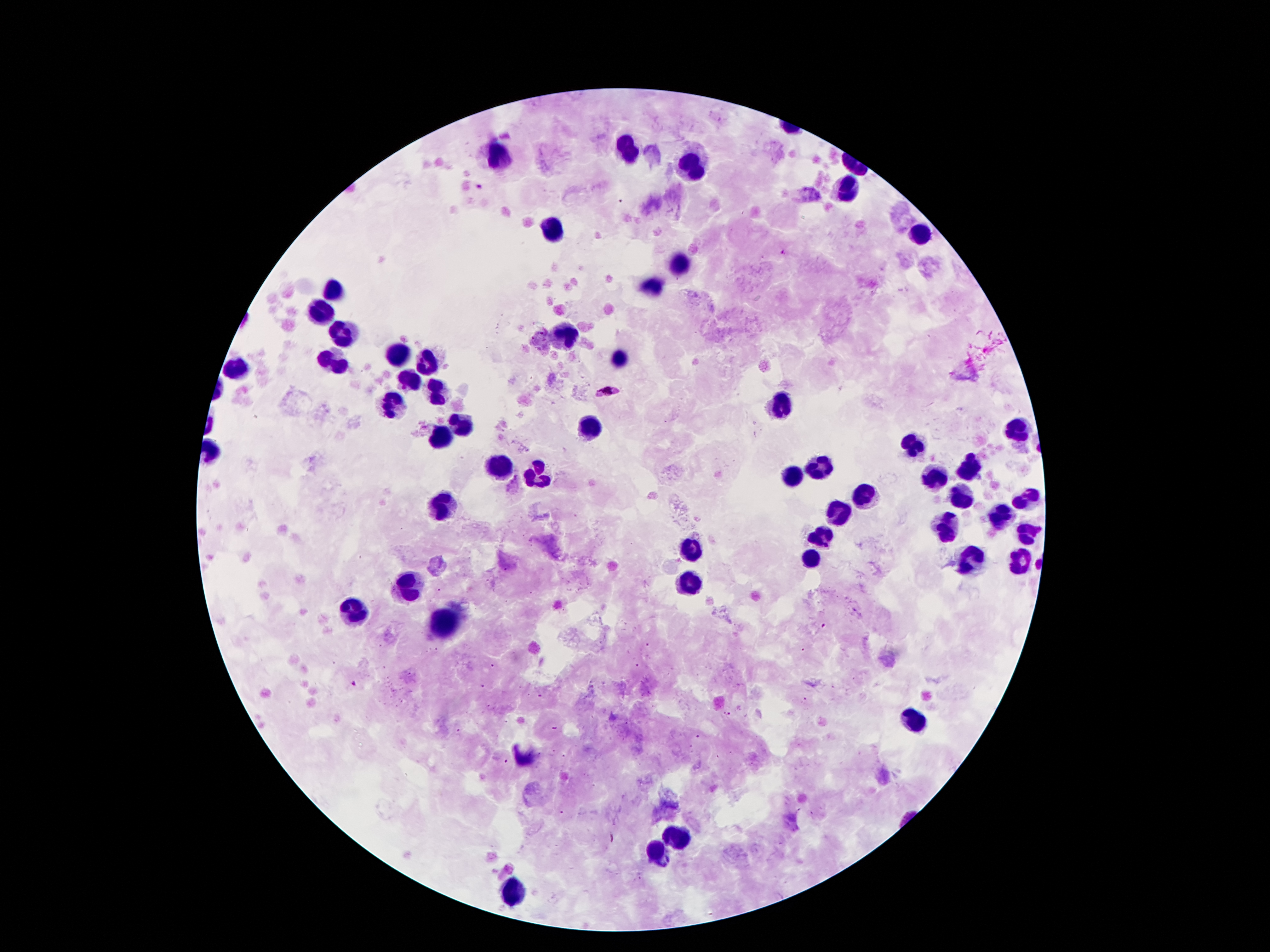
Approximate centers as [x, y] in pixels.
Summary:
  - Plasmodium parasite locations: [781, 254], [604, 386], [353, 685]
  - Leukocyte locations: [628, 150], [500, 156], [689, 166], [849, 192], [554, 227], [923, 234], [681, 263], [651, 286], [333, 291], [322, 313], [567, 333], [345, 336], [401, 357], [618, 361], [425, 362], [337, 364], [236, 369], [406, 383], [434, 389], [396, 406], [783, 407], [457, 428], [1017, 428], [592, 429], [439, 441], [911, 446], [501, 466], [819, 466], [969, 468], [534, 472], [793, 474], [933, 477], [862, 497], [962, 497], [1025, 499], [444, 505], [837, 510], [999, 516], [946, 522], [1027, 534], [822, 535], [691, 554], [811, 557], [972, 560], [1020, 560], [411, 588], [689, 588], [353, 615], [444, 621], [910, 718], [678, 838], [659, 853], [513, 896]
  - Image size: 1270×952 pixels
  - Preparation: thick blood film
  - Field of view: one from this slide
  - Stain: Giemsa
  - Capture: smartphone camera through the microscope eyepiece
  - Patient malaria status: positive for Plasmodium falciparum
  - Magnification: 100x